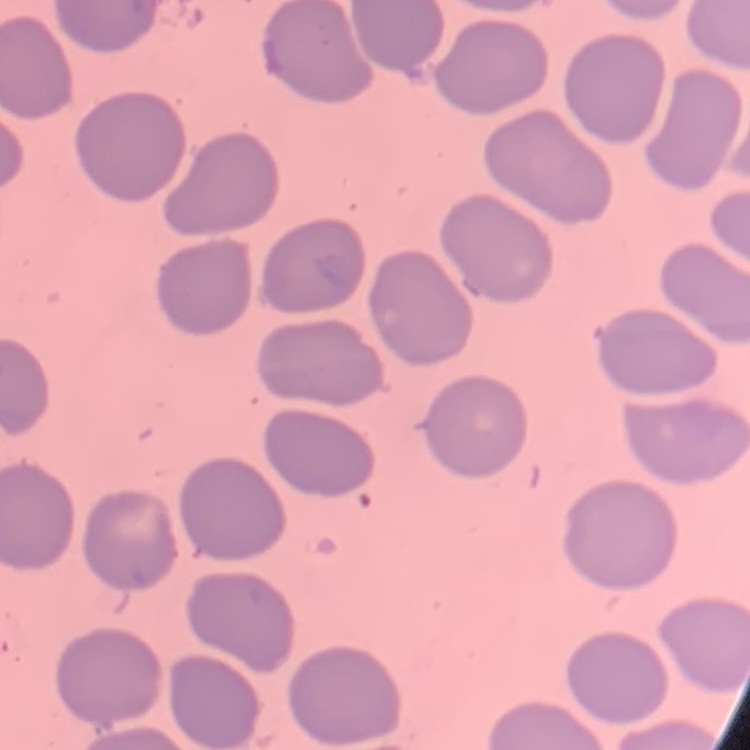 The erythrocytes show no rouleaux formation. Thin blood film. Square crop of a larger photomicrograph. Field's or Giemsa stain.